Locate every blood parasite and identify its species.
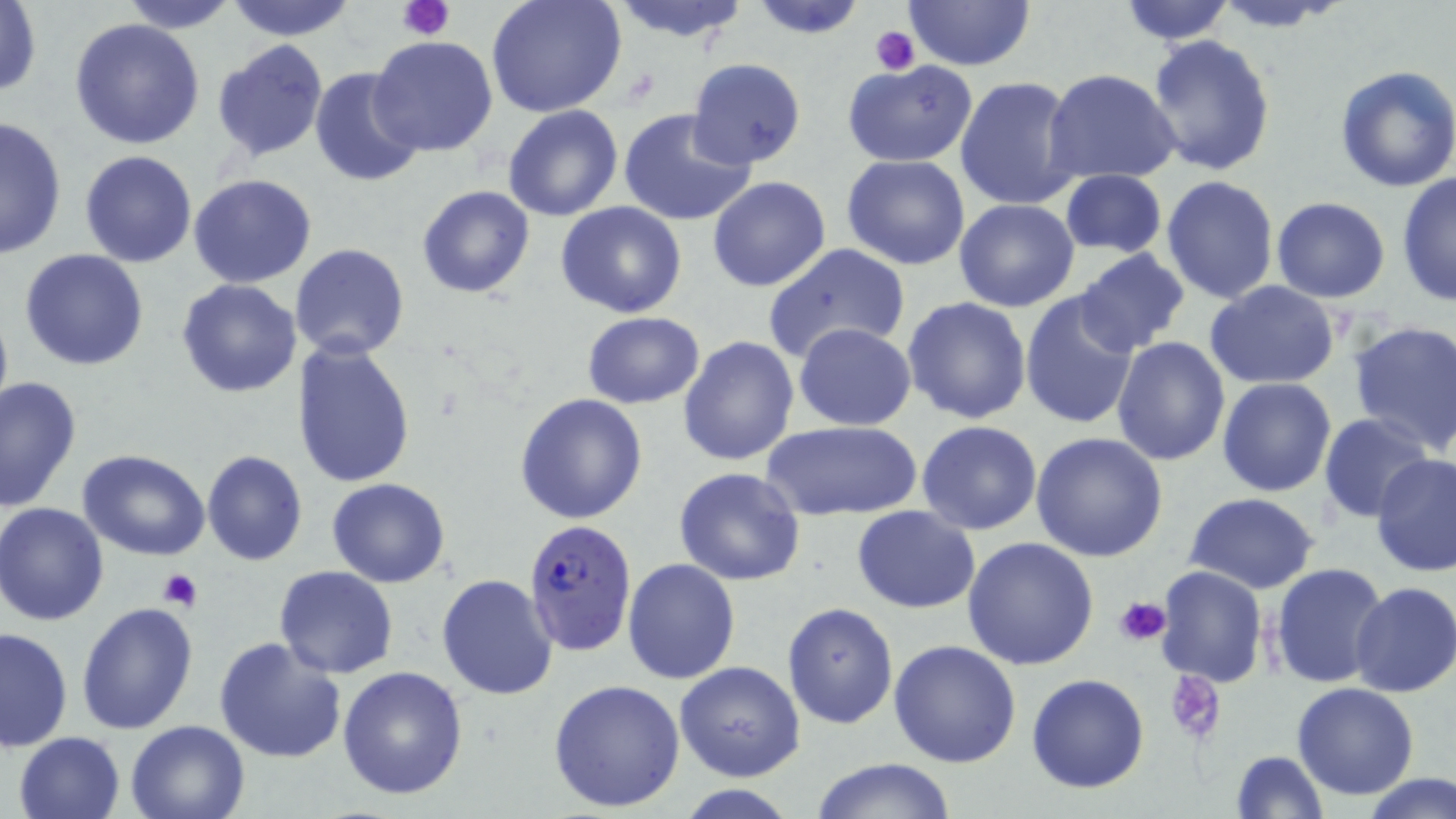

Approximate bounding boxes as (x1, y1, x2, y2) in pixels.
Plasmodium falciparum-infected red blood cells: (522, 519, 638, 658).
No Plasmodium ovale, Plasmodium malariae, Plasmodium vivax, Babesia divergens, or Trypanosoma brucei observed.

Uninfected red blood cell locations: (223, 0, 360, 40), (485, 0, 627, 118), (747, 0, 869, 38), (1116, 0, 1238, 45), (1210, 0, 1353, 32), (1, 1, 44, 100), (118, 1, 240, 32), (608, 1, 755, 44), (905, 1, 1035, 72), (69, 18, 205, 151), (1145, 34, 1278, 178), (366, 35, 498, 159), (213, 40, 329, 163), (685, 58, 808, 170), (843, 61, 977, 167), (1333, 64, 1456, 193), (310, 67, 425, 188), (1045, 69, 1182, 185), (954, 75, 1083, 213), (503, 105, 625, 222), (619, 108, 756, 226), (0, 115, 68, 258), (80, 149, 198, 267), (841, 155, 972, 271), (1058, 168, 1167, 259), (188, 173, 318, 289), (1396, 173, 1455, 306), (1161, 175, 1281, 304), (707, 176, 832, 292), (416, 185, 535, 298), (1271, 198, 1391, 303), (953, 199, 1079, 313), (556, 201, 687, 319), (290, 243, 409, 361), (762, 243, 909, 366), (19, 248, 150, 371), (1071, 249, 1191, 356), (176, 278, 303, 397), (1206, 279, 1341, 389), (1019, 289, 1143, 432), (0, 292, 13, 428), (903, 296, 1033, 425), (582, 311, 704, 409), (1347, 317, 1455, 457), (793, 323, 917, 431), (678, 336, 799, 466), (1111, 338, 1230, 466), (294, 341, 416, 489), (0, 375, 81, 512), (1217, 376, 1337, 496), (515, 392, 648, 524), (1319, 414, 1434, 523), (765, 420, 921, 521), (916, 421, 1042, 535), (1031, 432, 1168, 560), (78, 450, 212, 561), (203, 450, 308, 565), (1370, 453, 1456, 576), (673, 467, 806, 586), (327, 477, 450, 587), (1186, 493, 1318, 593), (1, 502, 112, 624), (852, 505, 980, 613), (962, 537, 1100, 670), (623, 558, 740, 684), (1270, 564, 1389, 688), (1154, 565, 1270, 686), (274, 566, 399, 678), (435, 573, 559, 701), (1350, 580, 1456, 699), (77, 602, 199, 736), (782, 603, 899, 729), (1, 626, 74, 752), (213, 634, 347, 764), (888, 640, 1022, 769), (675, 661, 805, 783), (338, 666, 469, 800), (1026, 673, 1149, 793), (548, 678, 687, 814), (1293, 683, 1420, 802), (125, 718, 252, 819), (14, 731, 126, 819), (1229, 750, 1328, 819), (810, 758, 959, 817), (1363, 775, 1456, 818), (673, 785, 802, 818). Platelet locations: (399, 0, 454, 40), (869, 25, 921, 74), (157, 567, 203, 611), (1113, 597, 1170, 646), (1164, 671, 1227, 745). Slide-level diagnosis: Plasmodium falciparum. Image is 1456×819 pixels. 1000x magnification. Single field of view. Thin blood film. May-Grünwald-Giemsa-stained preparation. Light microscopy.